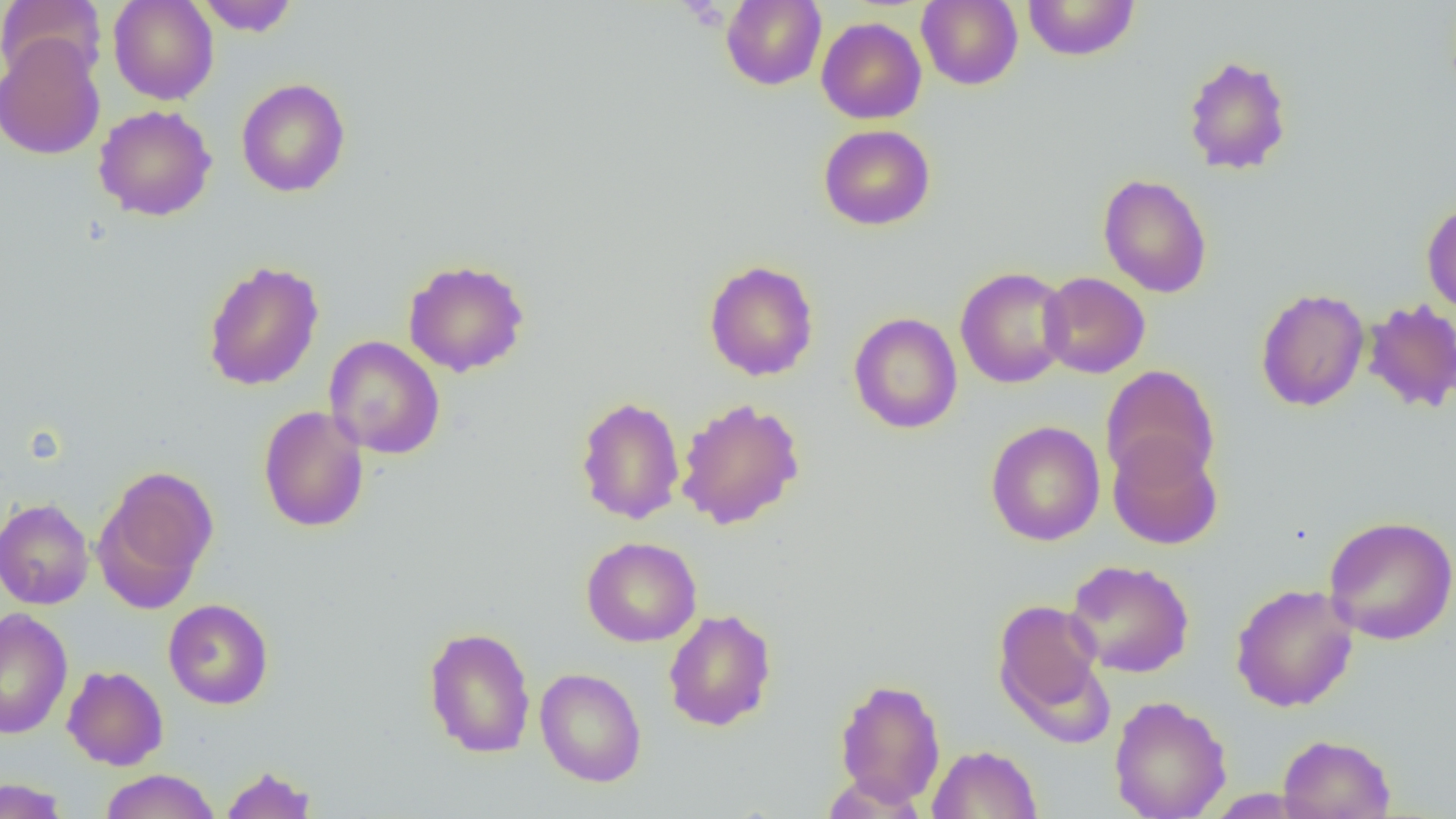
Approximate bounding boxes as (x1,y1)-(x2,y2) corner pairs in pixels. Uninfected red blood cell locations: (0,0)-(107,84), (108,0)-(218,105), (195,0)-(300,36), (721,0)-(827,91), (916,0)-(1023,90), (1022,0)-(1140,61), (816,17)-(927,124), (0,34)-(105,161), (1182,54)-(1293,175), (236,78)-(350,197), (93,104)-(217,221), (818,124)-(936,231), (1098,174)-(1213,298), (1422,200)-(1456,315), (403,259)-(530,377), (703,259)-(819,381), (202,260)-(324,391), (955,266)-(1072,388), (1038,272)-(1150,378), (1255,287)-(1370,412), (1361,299)-(1455,413), (848,312)-(963,434), (324,336)-(445,460), (1101,365)-(1220,486), (575,395)-(685,525), (675,397)-(805,531), (258,405)-(370,533), (985,420)-(1105,546), (1107,435)-(1222,550), (95,466)-(219,607), (0,498)-(95,610), (1324,515)-(1456,645), (581,536)-(702,647), (1065,559)-(1195,678), (1230,583)-(1359,712), (992,598)-(1108,724), (163,599)-(274,709), (0,608)-(73,740), (662,608)-(777,732), (423,626)-(536,758), (62,665)-(168,770), (534,667)-(647,787), (834,677)-(946,805), (1109,695)-(1232,819), (1277,733)-(1396,819), (928,745)-(1043,819), (219,764)-(318,819), (100,769)-(220,818), (0,778)-(71,818). Slide-level diagnosis: no evidence of blood parasites. Thin blood smear. Captured at 1000x magnification. One field of a larger specimen. Image is 1456×819 pixels. Light microscopy.